Assess this cell for malaria.
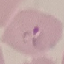
It is parasitized.

Acquired by smartphone through the microscope eyepiece. Thin smear of blood. Automatically extracted cell patch, resized to 64 × 64 pixels. Giemsa stain.